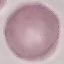

{
  "malaria_status": "uninfected",
  "preparation": "thin blood film",
  "capture": "smartphone through the microscope eyepiece",
  "stain": "Giemsa",
  "image_type": "cell patch, automatically extracted from a larger field of view and resized to 64 × 64 pixels"
}